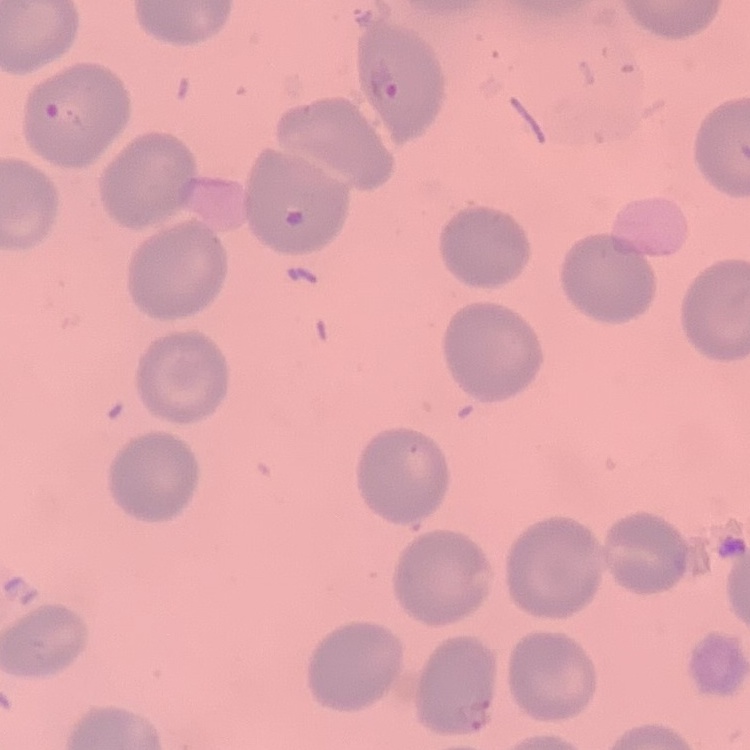
Summary:
  - Red blood cell morphology: no rouleaux formation
  - Image type: one tile cut from a larger photomicrograph
  - Stain: Field's or Giemsa
  - Preparation: thin blood smear